Assess this cell for malaria.
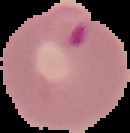

Parasitized.

Summary:
  - Preparation: thin blood smear
  - Image size: 130×133 pixels
  - Image type: segmented cell region on a black background